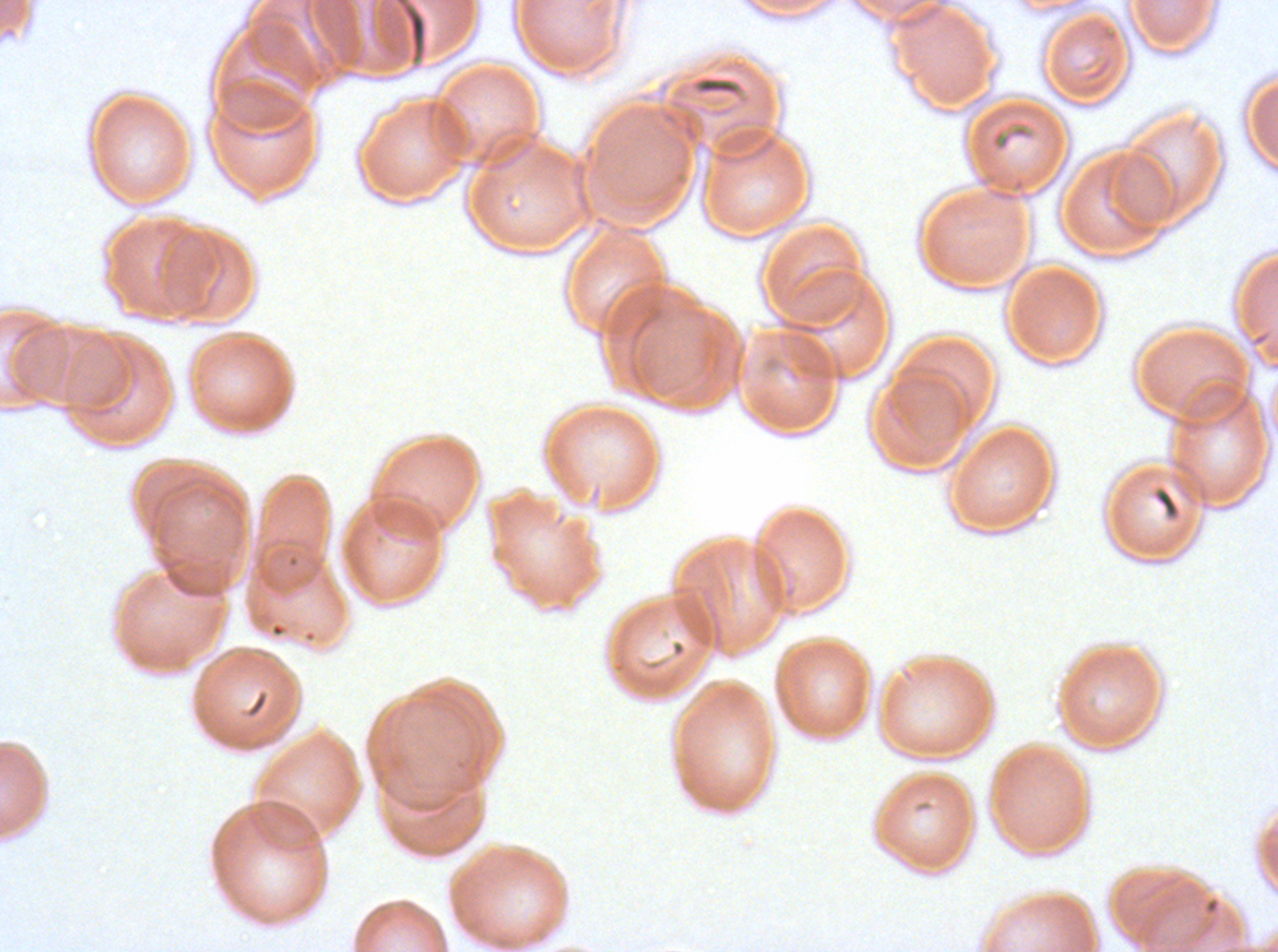

field_of_view: sub-image separated from a larger composite
preparation: thin blood film
stain: Giemsa
debris_locations: 'approximate bounding rectangles given as corner coordinates in pixels from the top-left: (x1=394, y1=0, x2=427, y2=55), (x1=694, y1=75, x2=742, y2=97), (x1=989, y1=124, x2=1034, y2=153), (x1=1153, y1=488, x2=1180, y2=519)'
image_size: 1278×952 pixels
specimen: P. falciparum cultured ex vivo for 24 to 48 hours, from a patient in The Gambia